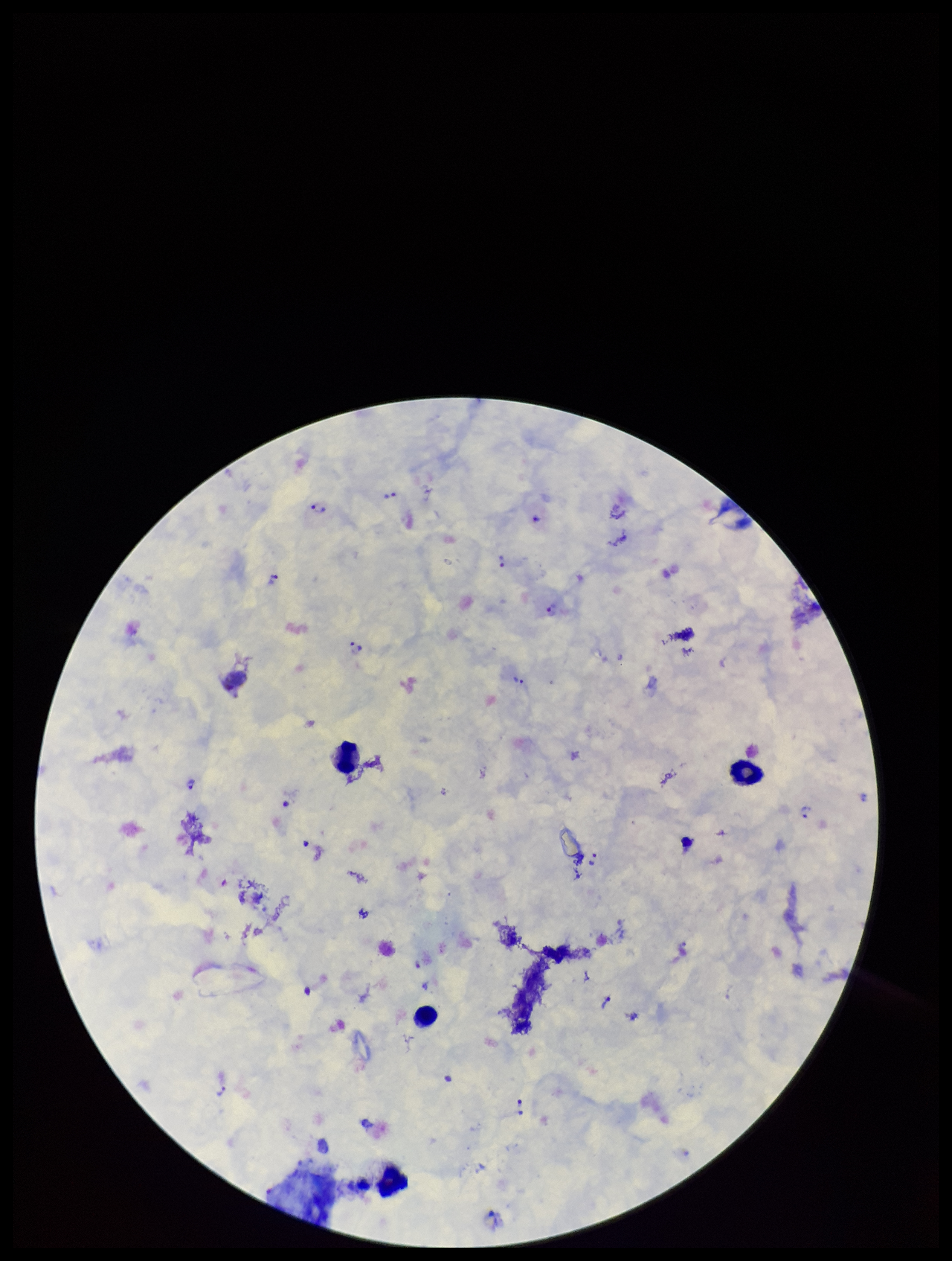 Preparation: thick smear. Smartphone photograph taken through the eyepiece of a microscope. Plasmodium parasites: identified. Species reported for this patient: Plasmodium vivax. Single field of view. Leukocyte count: 4. Patient malaria status: infected. Image is 952×1261 pixels. Giemsa stain. Parasite count: 20.